Describe the morphology of the erythrocytes.
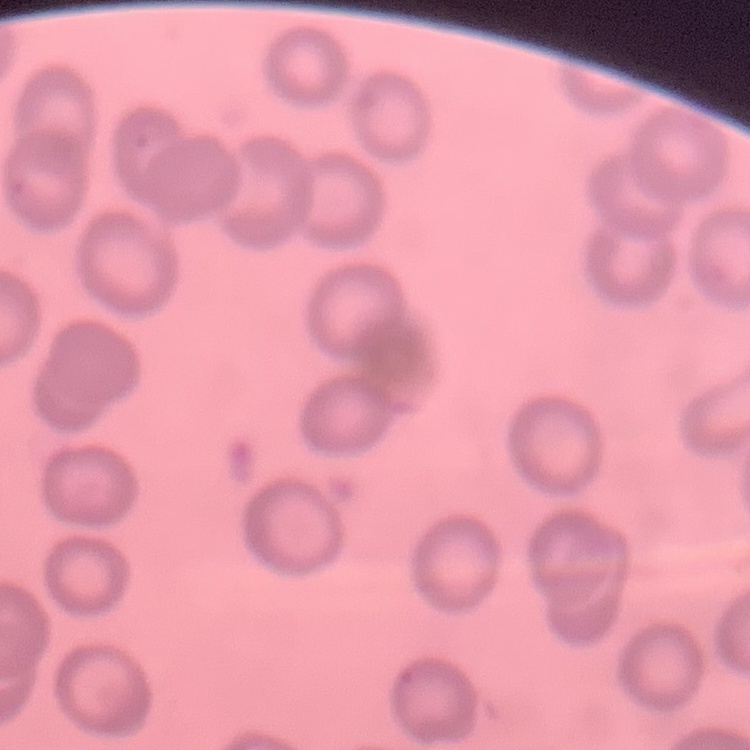
No rouleaux formation.

Summary:
  - Preparation: thin blood film
  - Image type: one tile cut from a larger photomicrograph
  - Stain: Field's or Giemsa